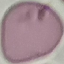
{
  "result": "no malaria parasites detected",
  "preparation": "thin smear",
  "image_type": "cell patch, automatically extracted from a larger field of view and resized to 64 × 64 pixels",
  "capture": "smartphone through the microscope eyepiece",
  "stain": "Giemsa"
}